Describe the morphology of the red blood cells.
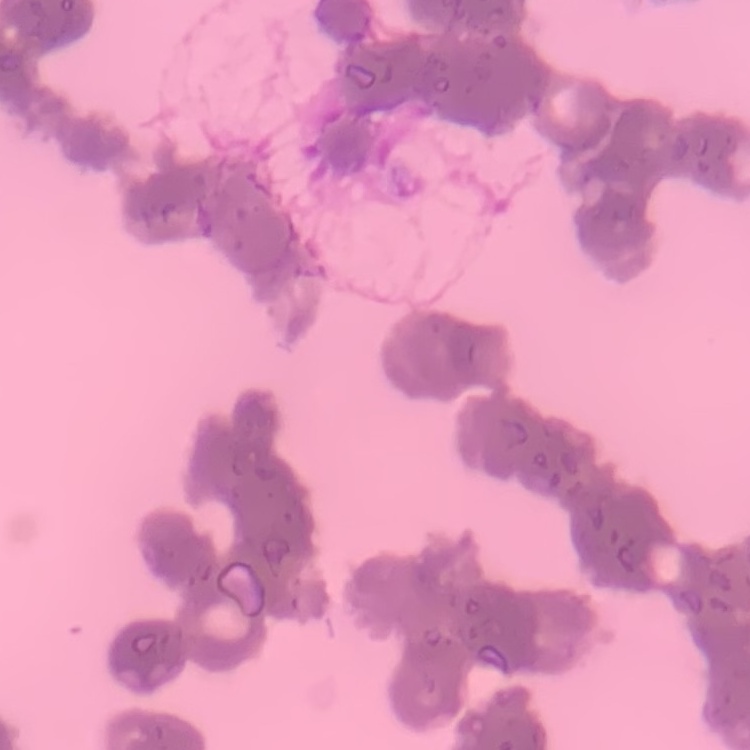

Rouleaux formation.

preparation = thin peripheral smear
stain = Field's or Giemsa
image type = square crop of a larger photomicrograph